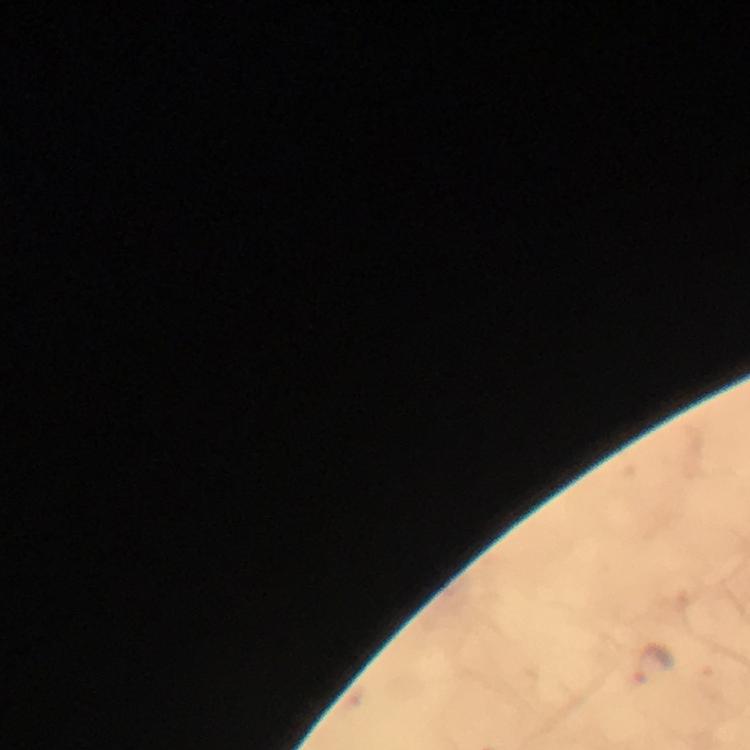

Approximate centers as {x, y} in pixels. Malaria parasite locations: {653, 663}. Giemsa-stained preparation. Immersion oil applied. Image is 750×750 pixels. Photographed with a smartphone mounted on the microscope. Thick smear. Cropped region of a single field of view. From a diagnostic examination for malaria. At 100x magnification.